Locate every uninfected red blood cell.
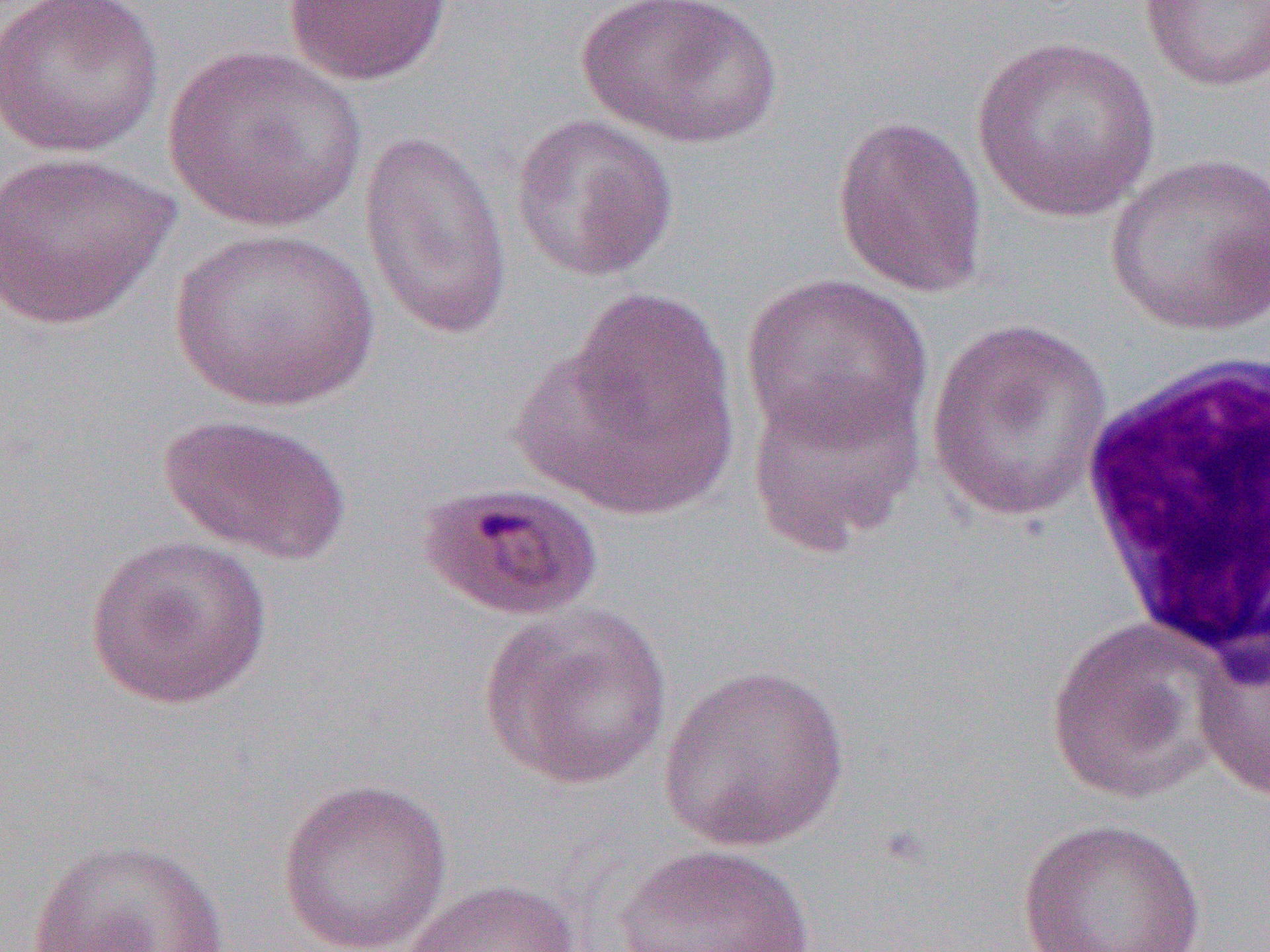
Approximate bounding boxes as named x1/y1/x2/y2 corners in pixels.
Uninfected red blood cells: (x1=1, y1=0, x2=164, y2=157), (x1=576, y1=0, x2=783, y2=149), (x1=1138, y1=0, x2=1270, y2=92), (x1=283, y1=1, x2=452, y2=86), (x1=969, y1=34, x2=1162, y2=225), (x1=162, y1=43, x2=367, y2=234), (x1=831, y1=112, x2=989, y2=299), (x1=510, y1=113, x2=678, y2=282), (x1=358, y1=128, x2=514, y2=343), (x1=0, y1=149, x2=179, y2=330), (x1=1103, y1=152, x2=1270, y2=337), (x1=167, y1=225, x2=382, y2=413), (x1=739, y1=273, x2=932, y2=451), (x1=521, y1=286, x2=746, y2=522), (x1=924, y1=318, x2=1117, y2=522), (x1=745, y1=375, x2=925, y2=556), (x1=158, y1=412, x2=351, y2=566), (x1=84, y1=533, x2=273, y2=711), (x1=477, y1=600, x2=673, y2=792), (x1=1043, y1=615, x2=1223, y2=804), (x1=1192, y1=632, x2=1270, y2=803), (x1=657, y1=662, x2=852, y2=852), (x1=276, y1=777, x2=454, y2=952), (x1=1017, y1=817, x2=1207, y2=952), (x1=26, y1=836, x2=232, y2=952), (x1=614, y1=844, x2=817, y2=951), (x1=398, y1=877, x2=582, y2=952).

slide-level diagnosis = Plasmodium malariae
field of view = one of a larger specimen
white blood cell locations = approximate bounding boxes as named x1/y1/x2/y2 corners in pixels: (x1=1076, y1=348, x2=1270, y2=665)
magnification = 1000x
image size = 1270×952 pixels
modality = optical microscopy
preparation = thin blood smear